Identify the blood parasite species.
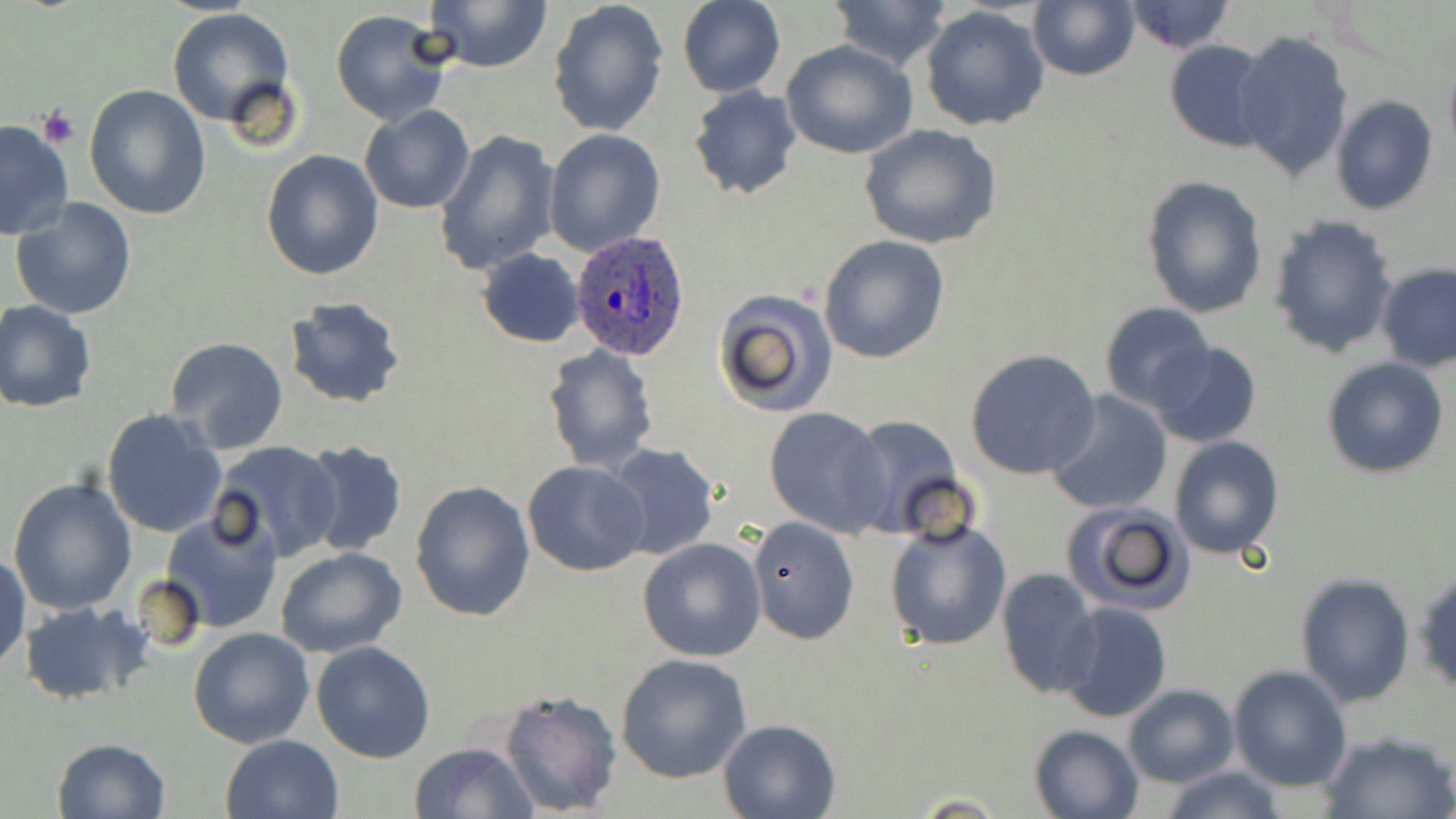

Plasmodium ovale.

Approximate bounding boxes as named x1/y1/x2/y2 corners in pixels. Plasmodium ovale-infected red blood cell locations: (x1=569, y1=231, x2=691, y2=359). Platelet locations: (x1=37, y1=108, x2=79, y2=149). Uninfected red blood cell locations: (x1=422, y1=0, x2=554, y2=74), (x1=546, y1=0, x2=669, y2=138), (x1=678, y1=0, x2=784, y2=98), (x1=828, y1=0, x2=955, y2=71), (x1=1028, y1=0, x2=1139, y2=81), (x1=1122, y1=0, x2=1236, y2=54), (x1=921, y1=5, x2=1049, y2=132), (x1=329, y1=8, x2=454, y2=127), (x1=167, y1=9, x2=295, y2=127), (x1=1233, y1=30, x2=1352, y2=186), (x1=1163, y1=38, x2=1275, y2=153), (x1=781, y1=40, x2=918, y2=161), (x1=1442, y1=51, x2=1456, y2=166), (x1=83, y1=83, x2=211, y2=220), (x1=687, y1=86, x2=803, y2=200), (x1=1329, y1=97, x2=1439, y2=214), (x1=359, y1=105, x2=475, y2=214), (x1=0, y1=118, x2=76, y2=241), (x1=860, y1=125, x2=1002, y2=248), (x1=544, y1=128, x2=665, y2=255), (x1=435, y1=129, x2=560, y2=276), (x1=260, y1=149, x2=384, y2=282), (x1=1142, y1=175, x2=1269, y2=320), (x1=10, y1=196, x2=138, y2=318), (x1=1269, y1=216, x2=1400, y2=358), (x1=818, y1=235, x2=950, y2=363), (x1=476, y1=249, x2=585, y2=348), (x1=1376, y1=263, x2=1456, y2=372), (x1=711, y1=289, x2=838, y2=416), (x1=283, y1=296, x2=406, y2=409), (x1=1, y1=301, x2=96, y2=415), (x1=1100, y1=303, x2=1216, y2=413), (x1=165, y1=338, x2=289, y2=455), (x1=1149, y1=341, x2=1262, y2=448), (x1=542, y1=344, x2=660, y2=474), (x1=965, y1=348, x2=1101, y2=480), (x1=1322, y1=357, x2=1450, y2=479), (x1=1044, y1=389, x2=1172, y2=515), (x1=764, y1=407, x2=894, y2=535), (x1=102, y1=408, x2=229, y2=540), (x1=845, y1=414, x2=966, y2=538), (x1=1169, y1=436, x2=1285, y2=558), (x1=298, y1=440, x2=408, y2=557), (x1=213, y1=441, x2=341, y2=560), (x1=604, y1=444, x2=721, y2=562), (x1=521, y1=461, x2=650, y2=577), (x1=8, y1=477, x2=139, y2=615), (x1=409, y1=480, x2=535, y2=622), (x1=1061, y1=500, x2=1197, y2=616), (x1=159, y1=505, x2=285, y2=636), (x1=748, y1=518, x2=860, y2=646), (x1=884, y1=519, x2=1012, y2=652), (x1=636, y1=539, x2=766, y2=661), (x1=276, y1=548, x2=406, y2=659), (x1=0, y1=552, x2=28, y2=672), (x1=996, y1=568, x2=1100, y2=697), (x1=1413, y1=568, x2=1456, y2=695), (x1=1295, y1=571, x2=1415, y2=707), (x1=20, y1=601, x2=149, y2=704), (x1=1057, y1=602, x2=1172, y2=723), (x1=188, y1=627, x2=314, y2=749), (x1=311, y1=641, x2=436, y2=763), (x1=614, y1=653, x2=752, y2=783), (x1=1228, y1=665, x2=1352, y2=791), (x1=1124, y1=684, x2=1239, y2=786), (x1=500, y1=689, x2=621, y2=817), (x1=717, y1=718, x2=840, y2=819), (x1=1028, y1=723, x2=1144, y2=819), (x1=1319, y1=729, x2=1455, y2=819), (x1=220, y1=734, x2=344, y2=819), (x1=51, y1=737, x2=171, y2=819), (x1=409, y1=741, x2=540, y2=819), (x1=1158, y1=764, x2=1287, y2=819). Image is 1456×819 pixels. May-Grünwald-Giemsa stain. One field of a larger specimen. 1000x magnification. Optical microscopy. Thin blood film.